Assess this cell for malaria.
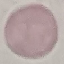
It is uninfected.

Giemsa stain. Acquired by smartphone through the microscope eyepiece. Cell patch, automatically extracted from a larger field of view and resized to 64 × 64 pixels. Thin smear of blood.